Report the malaria status of this cell.
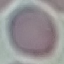
It is uninfected.

Thin blood smear. Automatically extracted cell patch, resized to 64 × 64 pixels. Photographed with a smartphone camera at the microscope eyepiece. Giemsa stain.